Locate every blood parasite and identify its species.
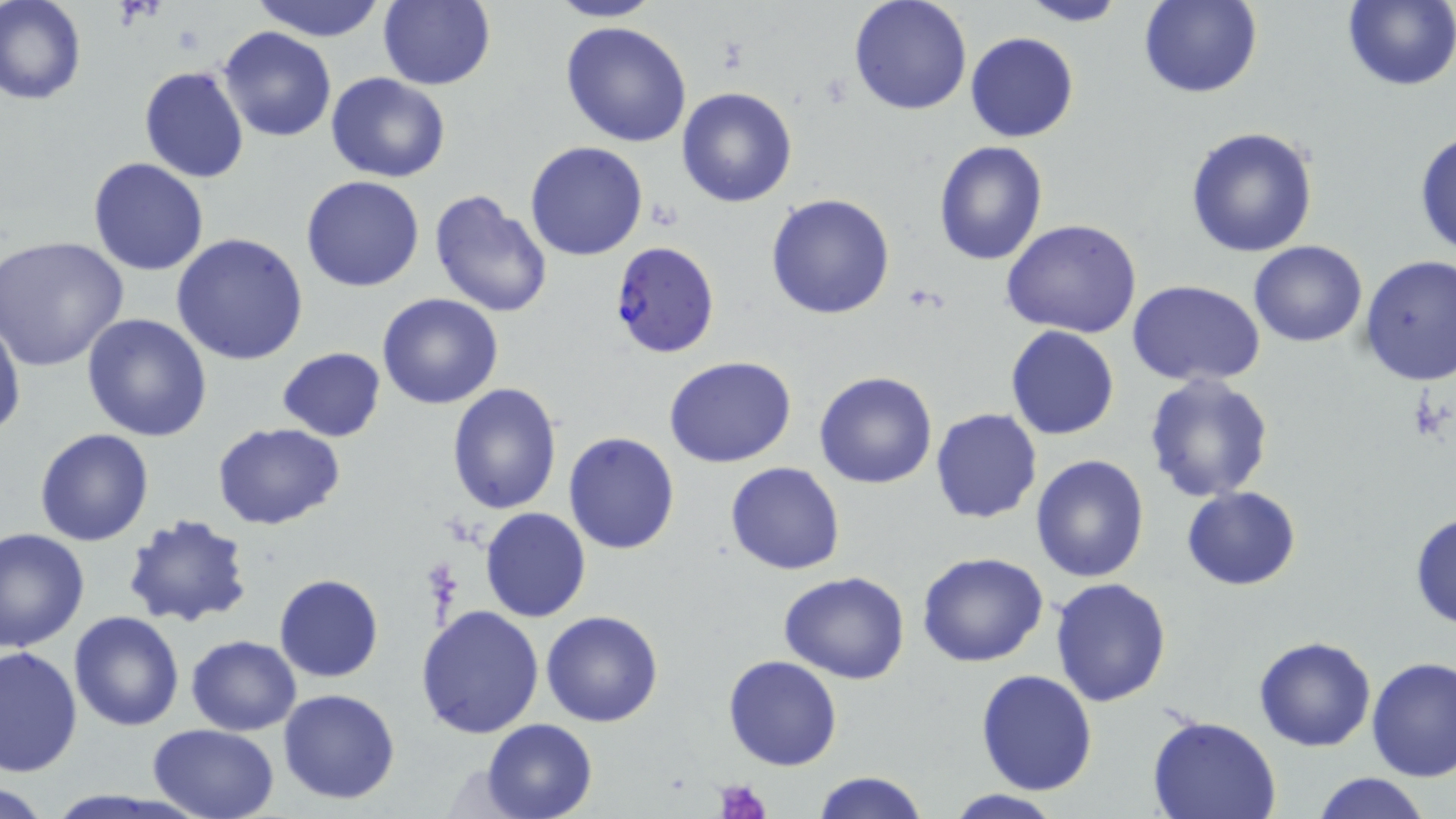
Approximate bounding boxes as (x1, y1, x2, y2) in pixels.
Plasmodium falciparum-infected red blood cells: (608, 239, 722, 358).
No Plasmodium ovale, Plasmodium malariae, Plasmodium vivax, Babesia divergens, or Trypanosoma brucei observed.

Uninfected red blood cell locations: (2, 0, 86, 105), (545, 0, 664, 22), (848, 0, 972, 116), (1019, 0, 1131, 26), (1138, 0, 1262, 98), (1342, 0, 1456, 92), (376, 1, 496, 90), (247, 2, 391, 41), (559, 20, 693, 148), (218, 27, 336, 143), (966, 32, 1079, 143), (139, 65, 250, 183), (327, 73, 451, 183), (677, 87, 797, 207), (1186, 126, 1319, 257), (1414, 130, 1456, 261), (525, 140, 649, 260), (932, 142, 1047, 266), (88, 157, 209, 275), (300, 175, 426, 292), (429, 187, 556, 318), (765, 193, 896, 320), (1000, 217, 1142, 338), (171, 232, 308, 365), (2, 237, 130, 372), (1247, 241, 1367, 347), (1358, 255, 1456, 385), (1127, 281, 1266, 383), (377, 294, 503, 410), (0, 308, 22, 444), (81, 312, 213, 442), (1005, 325, 1120, 441), (278, 347, 387, 441), (663, 354, 797, 468), (814, 370, 938, 489), (1143, 374, 1273, 502), (446, 383, 563, 516), (930, 408, 1042, 524), (212, 422, 344, 530), (34, 427, 156, 546), (564, 430, 680, 553), (1030, 453, 1150, 582), (724, 461, 845, 576), (1182, 486, 1300, 590), (480, 506, 591, 622), (121, 511, 255, 630), (1409, 511, 1456, 630), (0, 527, 90, 653), (916, 550, 1049, 668), (779, 571, 911, 684), (274, 574, 384, 682), (1050, 577, 1174, 707), (416, 605, 546, 740), (541, 609, 666, 727), (68, 611, 185, 730), (187, 635, 301, 735), (1253, 637, 1376, 751), (0, 645, 81, 778), (723, 655, 844, 771), (1366, 657, 1455, 782), (975, 669, 1099, 795), (277, 688, 401, 804), (1147, 715, 1279, 819), (479, 719, 599, 819), (147, 723, 280, 818), (812, 772, 929, 819), (1311, 772, 1434, 819), (1, 781, 56, 817), (941, 788, 1066, 819). Platelet locations: (718, 779, 771, 819). Slide-level diagnosis: Plasmodium falciparum. Thin blood film. Image is 1456×819 pixels. May-Grünwald-Giemsa-stained preparation. Single field of view. Optical microscopy. Captured at 1000x magnification.